Locate every leukocyte (white blood cell).
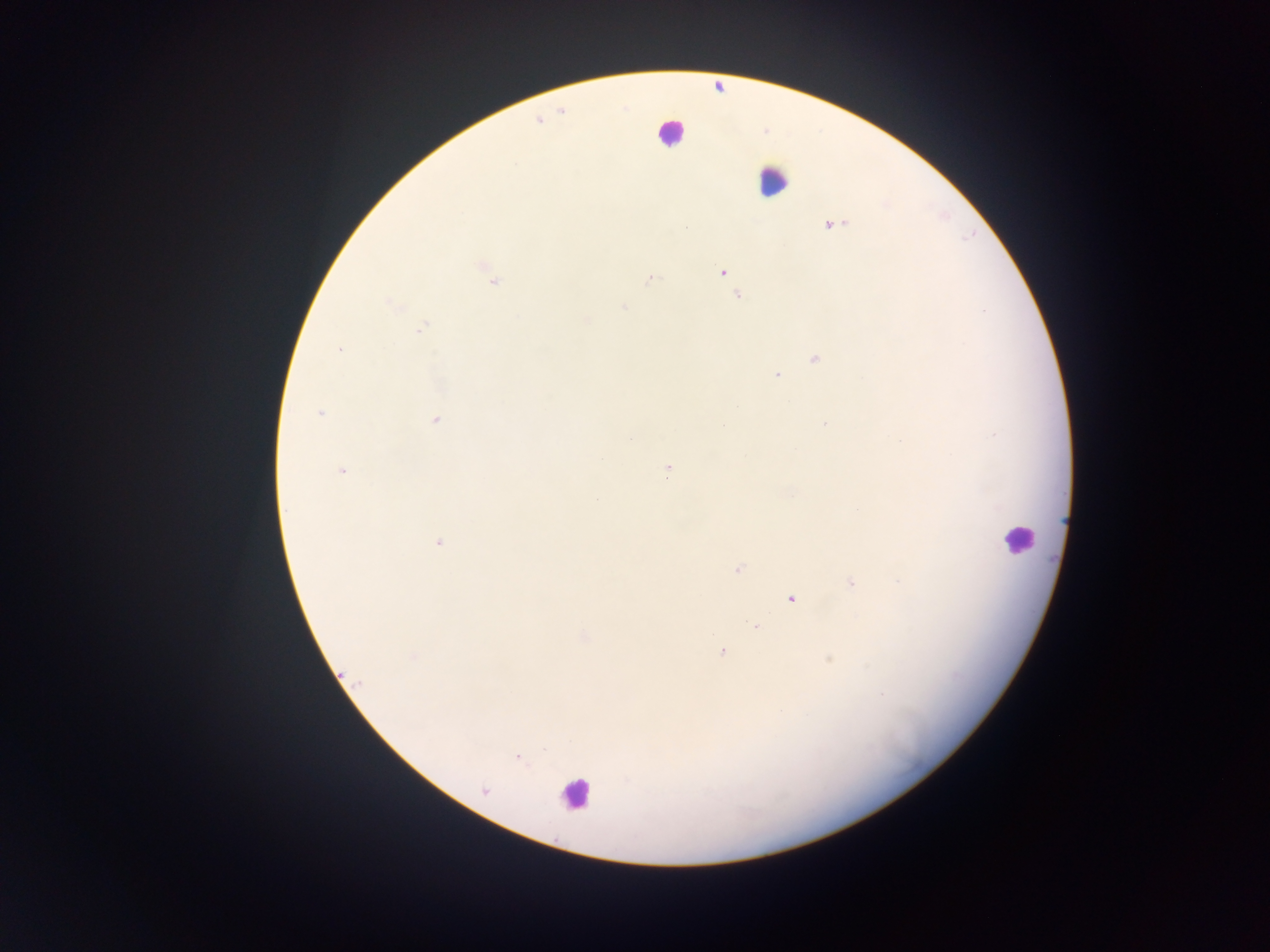
Approximate centers as [x, y] in pixels.
Leukocytes: [670, 131], [772, 180], [1017, 538], [574, 794].

field of view = single
preparation = thick blood film
image size = 1270×952 pixels
capture = mobile-phone photograph through a microscope
country = Ghana
malaria parasite locations = approximate centers as [x, y] in pixels: [834, 225], [485, 269], [723, 272], [650, 279], [491, 280], [737, 295], [392, 305], [623, 307], [983, 310], [586, 320], [422, 328], [339, 350], [815, 359], [776, 374], [320, 413], [436, 421], [824, 424], [631, 438], [601, 459], [667, 470], [342, 471], [438, 542], [738, 569], [851, 582], [791, 598], [754, 626], [722, 652], [414, 656], [829, 659], [518, 757], [484, 791]